State which parasite is depicted.
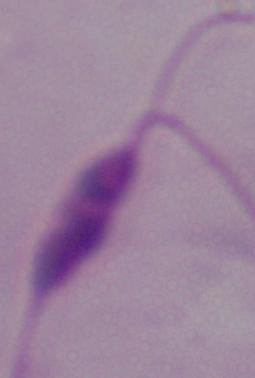
This is Leishmania.

Micrograph. 1000x magnification.